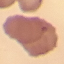

malaria status = uninfected
stain = Giemsa
image type = automatically extracted cell patch, resized to 64 × 64 pixels
preparation = thin blood film
capture = smartphone camera at the microscope eyepiece